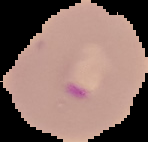
image type = cell region segmented out of the field of view; surrounding area masked to black
malaria status = parasitized
image size = 148×142 pixels
preparation = thin blood smear